Outline each blood parasite and name the species.
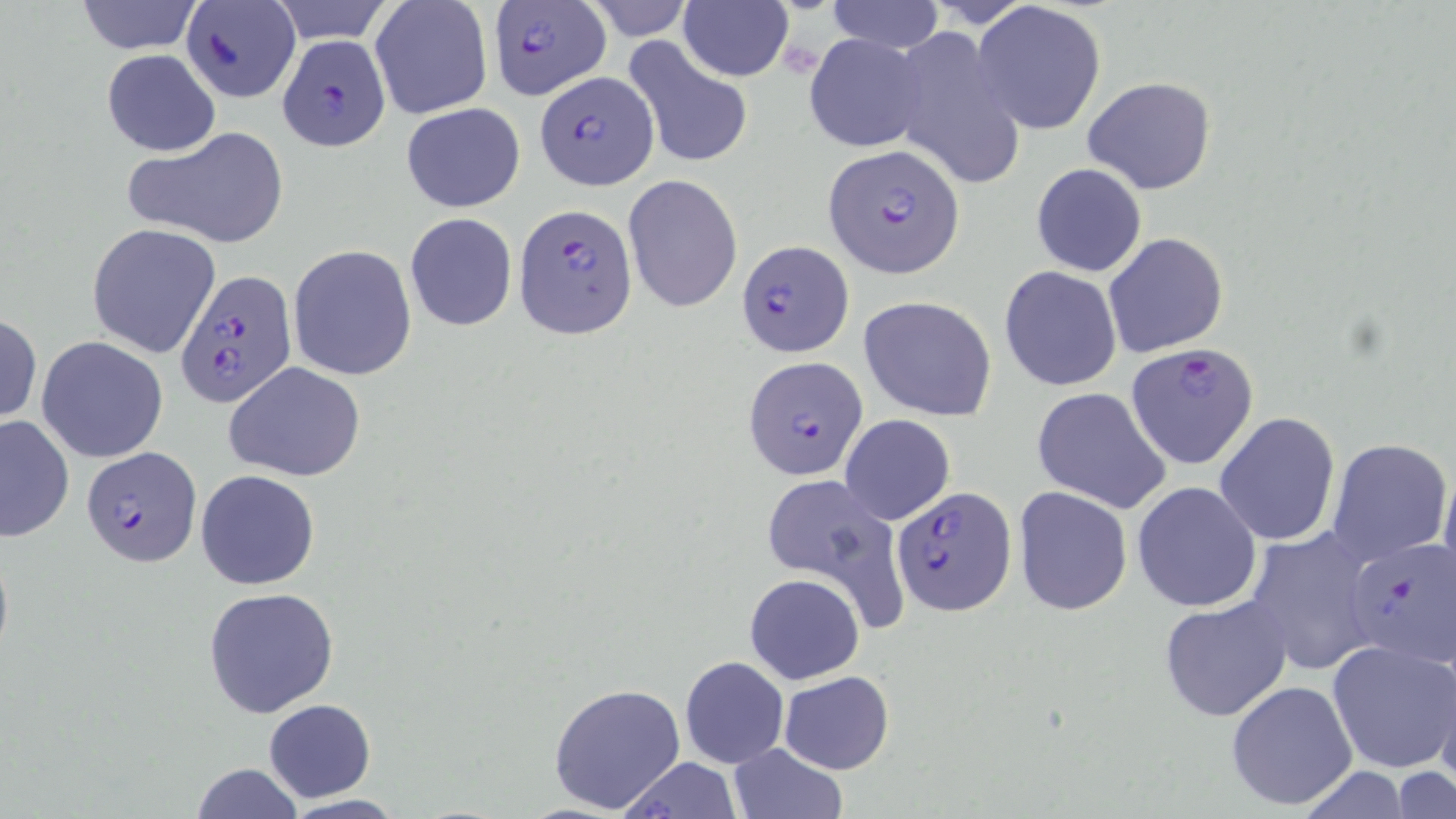
Approximate bounding boxes as (x1, y1, x2, y2) in pixels.
Plasmodium falciparum-infected red blood cells: (486, 0, 611, 102), (181, 3, 300, 101), (277, 33, 393, 149), (534, 70, 659, 190), (821, 144, 965, 277), (513, 202, 636, 337), (735, 238, 854, 356), (174, 268, 296, 409), (1125, 341, 1261, 471), (743, 355, 869, 481), (81, 447, 202, 568), (891, 485, 1015, 613), (1344, 537, 1456, 670).
No Plasmodium ovale, Plasmodium malariae, Plasmodium vivax, Babesia divergens, or Trypanosoma brucei observed.

slide-level diagnosis = Plasmodium falciparum
field of view = one of a larger specimen
stain = May-Grünwald-Giemsa
image size = 1456×819 pixels
magnification = 1000x
modality = light microscopy
uninfected red blood cell locations = approximate bounding boxes as (x1, y1, x2, y2) in pixels: (71, 0, 205, 53), (579, 0, 696, 41), (825, 0, 944, 54), (267, 1, 397, 46), (369, 1, 494, 121), (679, 2, 793, 82), (975, 2, 1107, 133), (889, 24, 1025, 196), (803, 33, 929, 153), (621, 38, 756, 171), (102, 49, 220, 157), (1084, 76, 1217, 195), (399, 102, 525, 212), (121, 128, 291, 249), (1030, 163, 1147, 278), (624, 175, 743, 312), (405, 213, 517, 331), (86, 223, 220, 358), (1103, 231, 1228, 358), (287, 245, 417, 380), (999, 265, 1122, 392), (859, 295, 997, 420), (0, 311, 41, 427), (36, 336, 168, 463), (224, 362, 367, 482), (1031, 386, 1172, 514), (1214, 412, 1341, 547), (0, 414, 74, 542), (839, 414, 955, 525), (1327, 437, 1452, 565), (1440, 464, 1455, 596), (194, 469, 321, 591), (759, 469, 910, 631), (1132, 481, 1263, 614), (1012, 486, 1133, 615), (1244, 526, 1380, 677), (744, 573, 865, 685), (203, 587, 340, 720), (1159, 598, 1293, 723), (1328, 639, 1456, 774), (679, 656, 789, 768), (778, 671, 894, 774), (1226, 679, 1358, 811), (547, 681, 687, 816), (262, 699, 376, 802), (728, 742, 848, 819), (617, 758, 746, 817), (190, 763, 305, 818), (1391, 767, 1456, 819)
preparation = thin blood smear